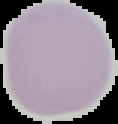
preparation: thin blood film
image_type: segmented cell region with the area outside set to black
malaria_status: uninfected
image_size: 118×124 pixels